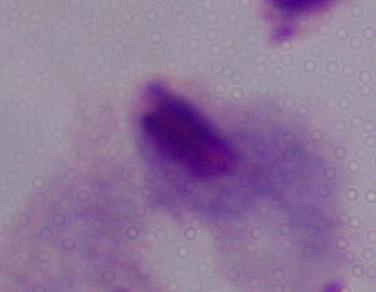
Summary:
  - Magnification: 1000x
  - Modality: photomicrograph
  - Identification: trichomonad